Report the malaria status of this cell.
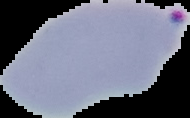

It is parasitized.

Summary:
  - Image type: segmented cell region on a black background
  - Image size: 190×118 pixels
  - Preparation: thin blood smear